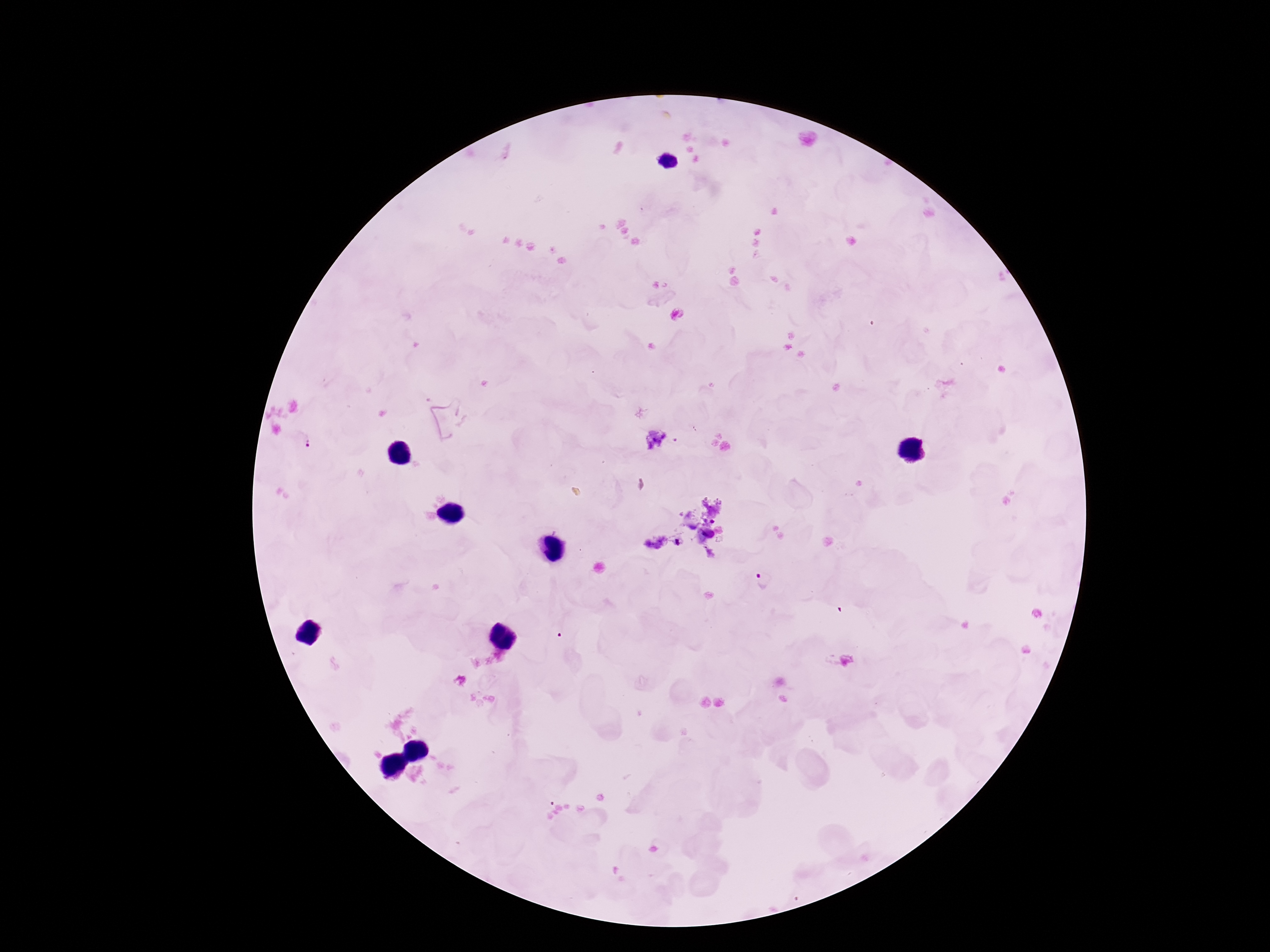

stain = Giemsa
field of view = one from this slide
magnification = 100x
patient malaria status = infected
capture = smartphone camera through the microscope eyepiece
image size = 1270×952 pixels
Plasmodium parasite locations = approximate centers as (x, y) in pixels: (301, 441), (765, 580)
preparation = thick peripheral-blood smear